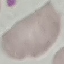

result: no malaria parasites seen
stain: Giemsa
capture: smartphone camera at the microscope eyepiece
preparation: thin blood film
image_type: automatically extracted cell patch, resized to 64 × 64 pixels